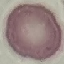
malaria_status: uninfected
image_type: cell patch, automatically extracted from a larger field of view and resized to 64 × 64 pixels
capture: smartphone through the microscope eyepiece
preparation: thin smear
stain: Giemsa